Name the parasite shown.
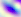

Toxoplasma gondii.

{
  "modality": "photomicrograph",
  "magnification": "400x"
}